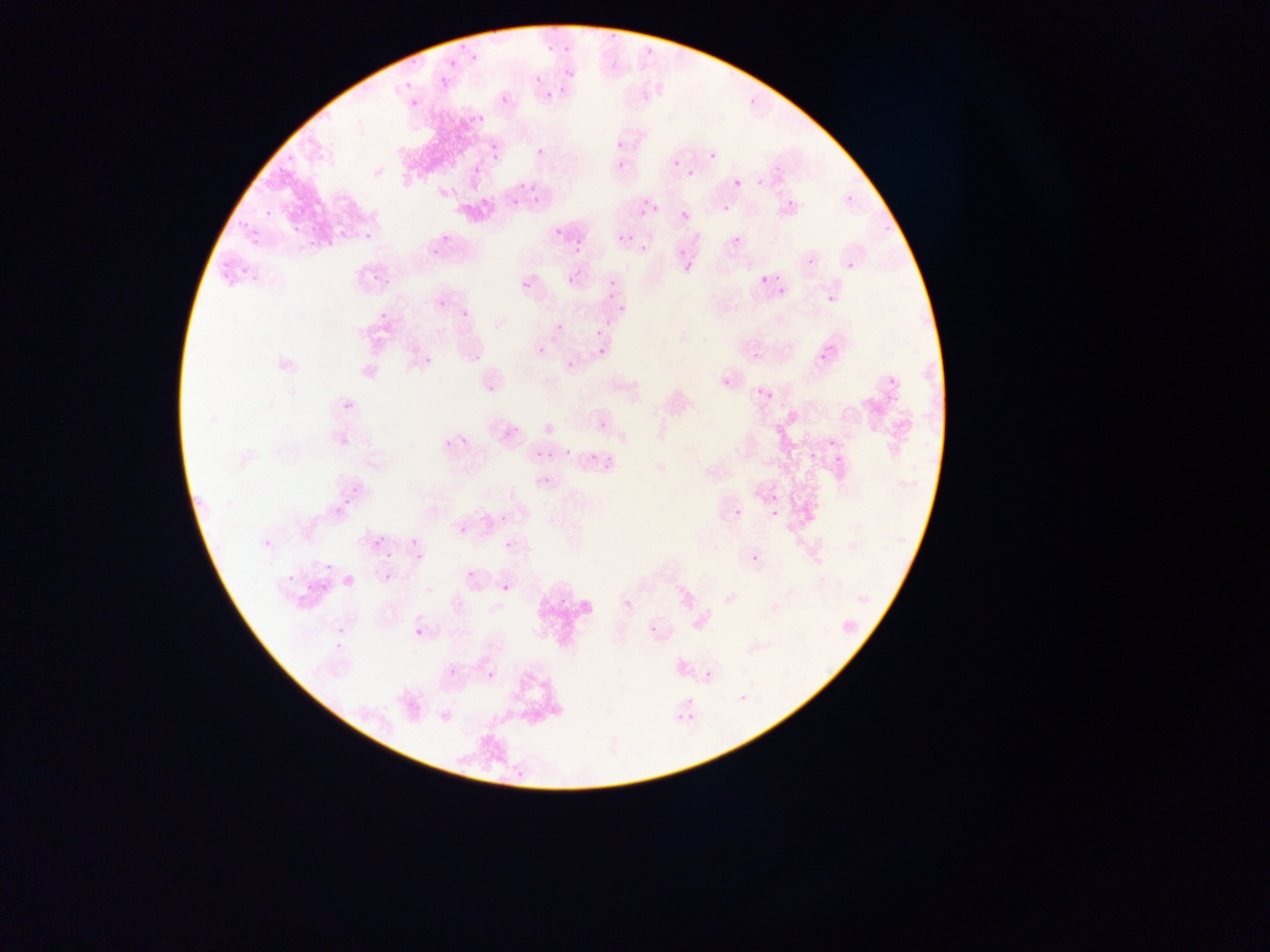
Approximate bounding boxes as [left, top, right, bottom] in pixels.
Summary:
  - Plasmodium parasite locations: [608, 28, 618, 41], [563, 39, 573, 53], [545, 40, 555, 56], [456, 43, 466, 50], [467, 51, 481, 68], [408, 54, 419, 69], [446, 58, 456, 66], [560, 63, 579, 84], [434, 76, 449, 87], [400, 84, 410, 92], [541, 84, 559, 102], [501, 95, 509, 104], [746, 98, 756, 109], [408, 101, 424, 111], [479, 108, 487, 128], [469, 117, 475, 125], [608, 134, 625, 152], [491, 141, 502, 150], [533, 142, 547, 159], [706, 148, 715, 165], [615, 156, 628, 170], [672, 159, 680, 166], [473, 165, 482, 175], [687, 170, 695, 177], [519, 179, 533, 193], [734, 179, 742, 186], [639, 195, 653, 209], [783, 195, 798, 210], [846, 195, 854, 203], [531, 196, 544, 205], [511, 198, 519, 205], [722, 204, 730, 213], [634, 207, 659, 225], [263, 208, 271, 218], [680, 212, 688, 220], [230, 216, 251, 234], [290, 221, 302, 237], [548, 223, 568, 241], [357, 224, 376, 241], [250, 227, 263, 247], [339, 227, 349, 241], [306, 229, 321, 248], [620, 235, 630, 243], [733, 235, 742, 244], [322, 236, 337, 247], [431, 236, 444, 261], [572, 241, 583, 256], [672, 245, 689, 258], [640, 246, 648, 253], [844, 258, 859, 269], [802, 260, 811, 270], [367, 261, 387, 283], [237, 262, 247, 279], [217, 263, 229, 280], [682, 264, 692, 277], [562, 266, 583, 286], [245, 271, 258, 287], [608, 273, 622, 288], [760, 275, 768, 284], [523, 281, 532, 290], [778, 287, 786, 296], [825, 292, 835, 302], [603, 293, 618, 301], [437, 300, 446, 309], [457, 304, 477, 321], [615, 305, 628, 313], [380, 312, 389, 320], [605, 320, 615, 331], [555, 323, 563, 331], [591, 325, 607, 338], [537, 347, 545, 355], [469, 348, 488, 361], [598, 349, 606, 357], [818, 351, 829, 365], [751, 353, 760, 362], [424, 356, 432, 365], [566, 360, 574, 368], [883, 376, 887, 389], [483, 381, 500, 403], [757, 388, 768, 398], [764, 390, 774, 400], [340, 401, 355, 413], [498, 415, 525, 442], [599, 422, 607, 431], [459, 431, 472, 449], [443, 437, 453, 448], [825, 438, 835, 449], [734, 444, 744, 453], [733, 446, 740, 454], [806, 447, 822, 461], [604, 448, 616, 473], [563, 449, 573, 458], [535, 451, 542, 460], [589, 453, 602, 463], [832, 453, 845, 467], [539, 476, 551, 486], [769, 493, 779, 501], [341, 496, 352, 510], [334, 501, 348, 514], [334, 507, 344, 517], [734, 508, 742, 517], [770, 509, 778, 517], [500, 515, 507, 523], [458, 526, 467, 536], [263, 534, 275, 551], [372, 537, 383, 547], [409, 538, 419, 548], [504, 542, 512, 550], [382, 548, 392, 564], [414, 553, 424, 564], [751, 554, 761, 563], [322, 562, 333, 574], [384, 566, 394, 580], [283, 569, 299, 588], [466, 570, 475, 579], [303, 577, 313, 602], [322, 581, 328, 596], [502, 583, 510, 591], [623, 598, 633, 609], [335, 624, 350, 645], [648, 625, 657, 635], [414, 629, 423, 636], [702, 669, 713, 678], [705, 671, 711, 679], [487, 672, 495, 681], [739, 694, 746, 702] | approximate [x, y] pixel centers of objects too small to bound: [537, 79], [225, 286]
  - Image size: 1270×952 pixels
  - Capture: mobile-phone photograph through a microscope
  - Country: Ghana
  - Field of view: single
  - Preparation: thin blood film